Locate every Plasmodium parasite.
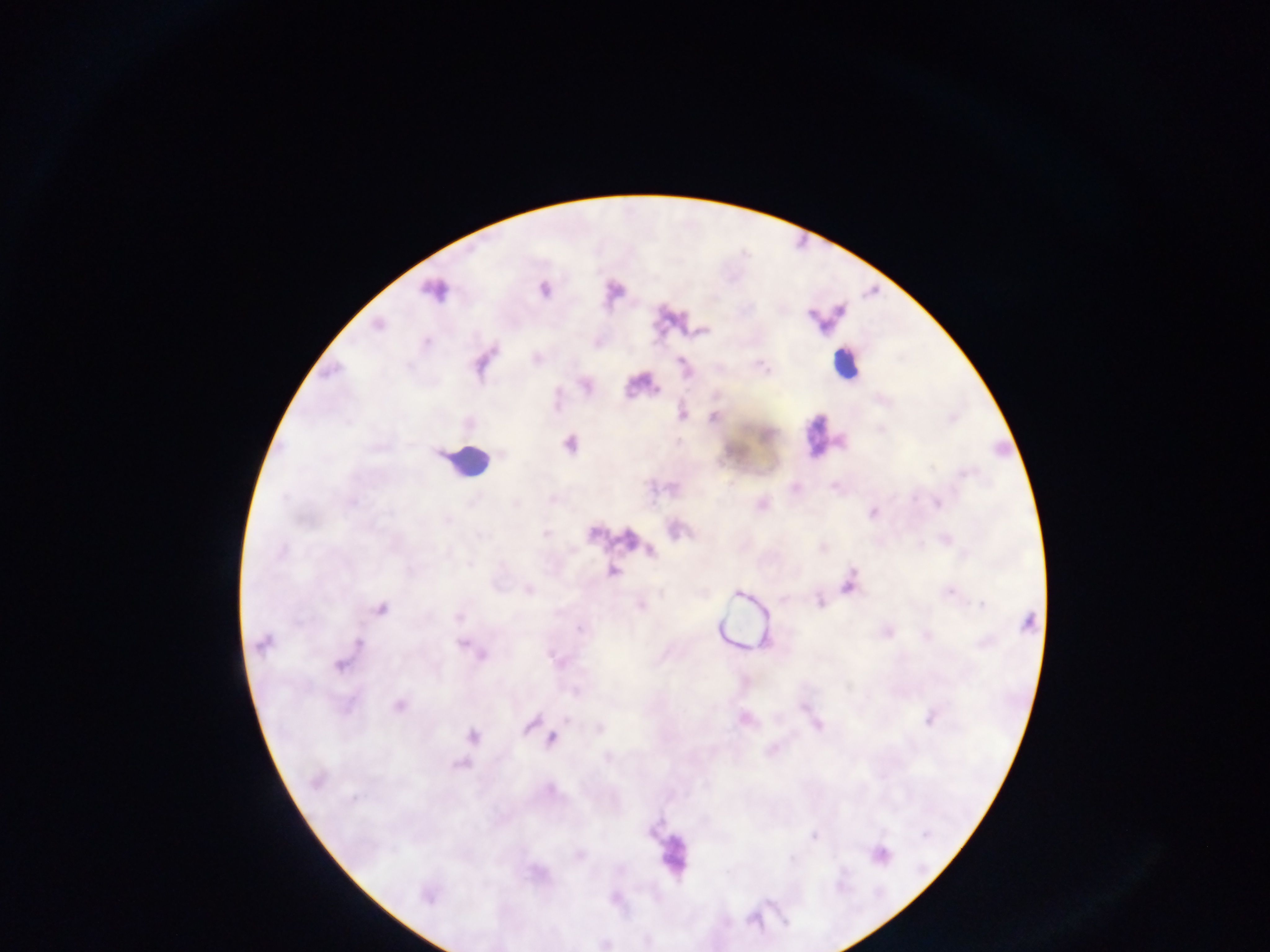

Approximate centers as x y in pixels.
Plasmodium parasites: 435 289; 543 290; 613 290; 377 324; 700 331; 536 358; 585 385; 681 414; 713 417; 569 443; 795 488; 937 502; 762 504; 873 512; 675 530; 629 538; 822 547; 650 551; 612 572; 849 583; 528 589; 738 593; 819 601; 640 604; 380 608; 1028 623; 886 631; 264 642; 475 651; 343 661; 398 705; 931 717; 743 718; 815 723; 531 725; 598 728; 472 736; 551 738; 458 764; 316 780; 813 836; 880 854; 536 872; 428 894; 615 898; 604 943.

Leukocyte locations: 845 363; 818 435; 467 462; 673 854. Image is 1270×952 pixels. Thick blood film. One field of view. Mobile-phone photograph taken through the microscope. Collected in Ghana.